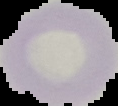
Summary:
  - Preparation: thin blood smear
  - Image size: 118×106 pixels
  - Malaria status: uninfected
  - Image type: segmented cell region on a black background